Locate every uninfected red blood cell.
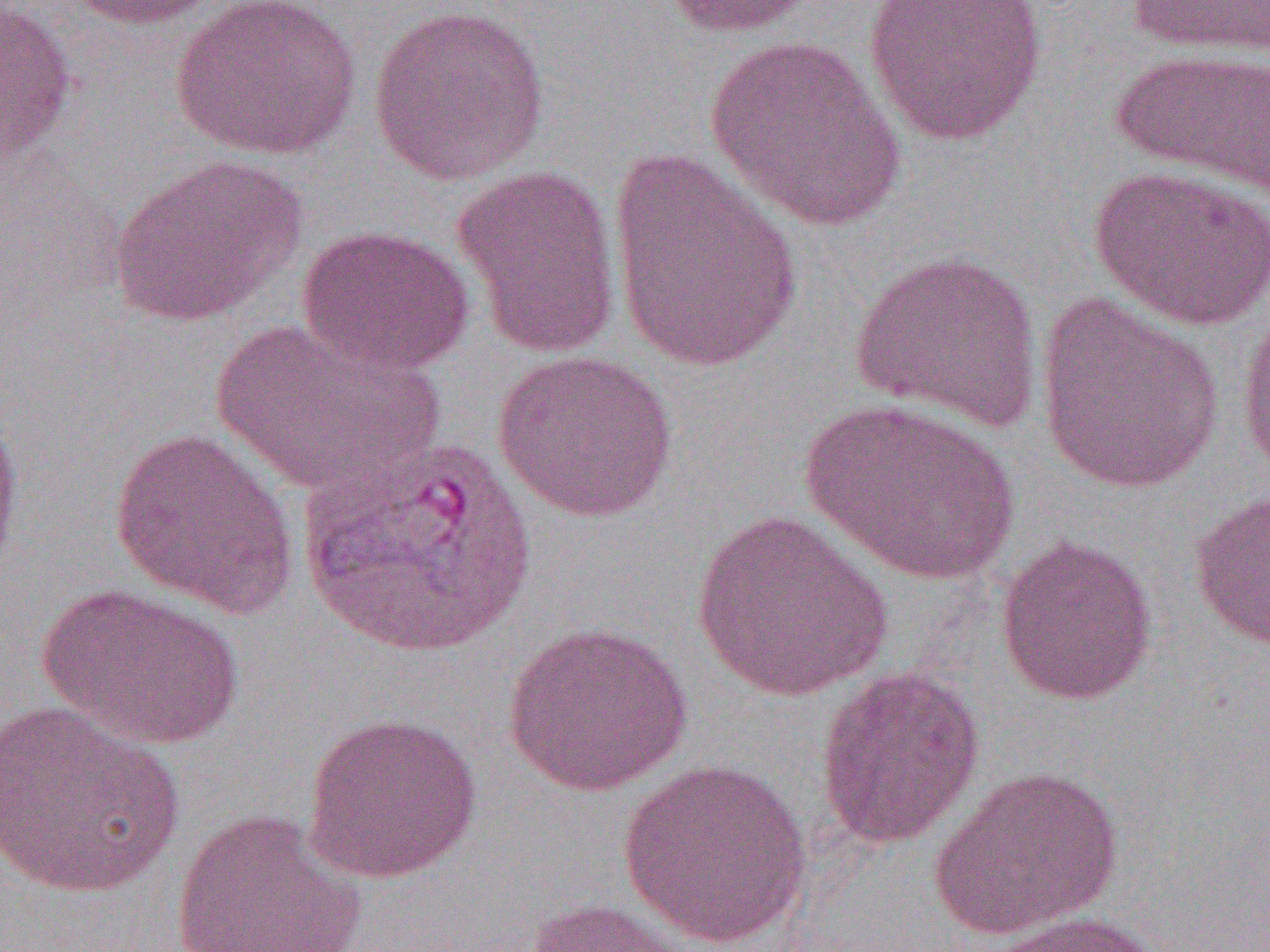

Approximate bounding boxes as (x1,y1)-(x2,y2) corner pairs in pixels.
Uninfected red blood cells: (66,0)-(222,30), (169,0)-(362,159), (655,0)-(822,39), (863,0)-(1049,146), (1125,0)-(1270,58), (1,3)-(77,171), (368,4)-(551,186), (704,36)-(906,230), (1111,47)-(1270,198), (606,149)-(806,373), (107,153)-(308,328), (451,163)-(623,359), (1090,165)-(1270,331), (295,223)-(475,376), (849,249)-(1044,432), (1034,292)-(1226,494), (1236,301)-(1270,484), (210,319)-(442,499), (491,349)-(679,522), (802,398)-(1019,585), (0,401)-(24,590), (109,427)-(299,619), (1188,487)-(1270,652), (690,508)-(894,703), (995,534)-(1158,705), (37,583)-(244,751), (501,622)-(693,796), (814,664)-(985,850), (0,701)-(185,897), (301,711)-(483,884), (617,757)-(814,948), (930,765)-(1123,940), (169,808)-(370,952), (525,897)-(697,952), (983,911)-(1171,952).

Summary:
  - Slide-level diagnosis: Plasmodium vivax
  - Image size: 1270×952 pixels
  - Field of view: one of a larger specimen
  - Magnification: 1000x
  - Preparation: thin blood smear
  - Modality: optical microscopy